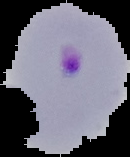 The area outside the segmented cell region is set to black. From a thin blood film. Result: Plasmodium parasites detected. Image is 130×157 pixels.